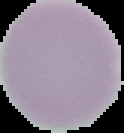 The area outside the segmented cell region is set to black. From a thin blood smear. Malaria status: uninfected. Image is 124×133 pixels.